Assess the morphology of the erythrocytes.
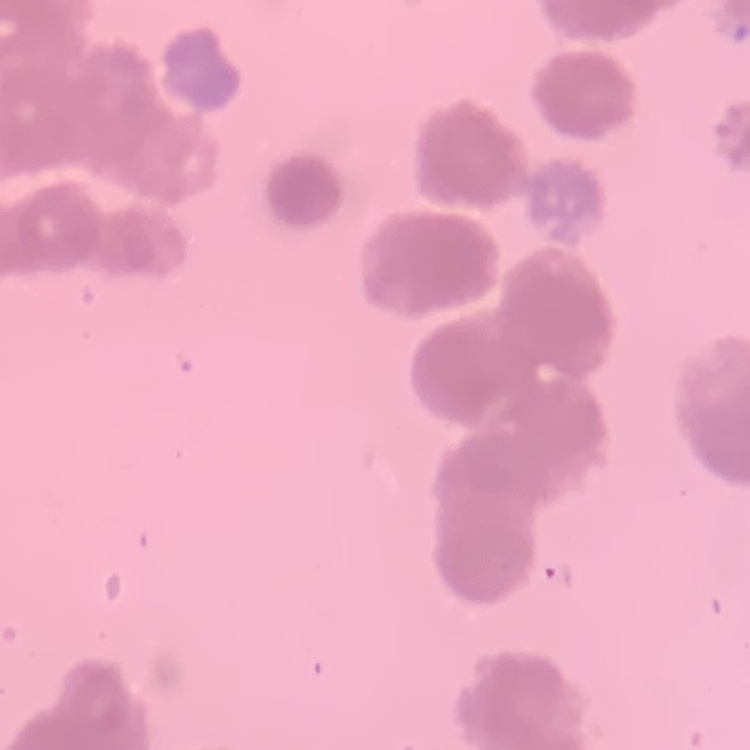
Rouleaux formation.

Summary:
  - Preparation: thin peripheral smear
  - Stain: Field's or Giemsa
  - Image type: square crop of a larger photomicrograph